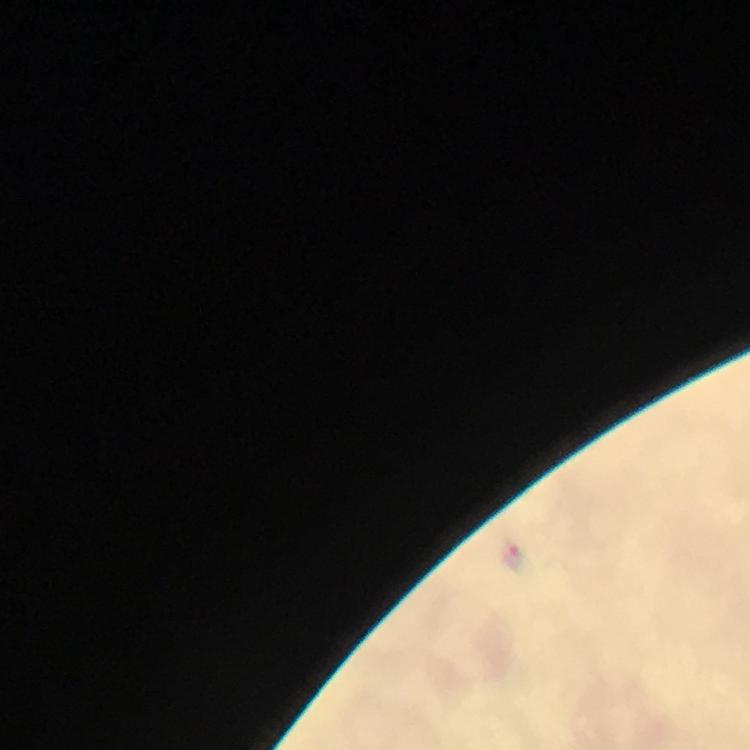

cropped from = one field of view
immersion oil = used
context = from a malaria diagnostic workup
preparation = thick blood film
malaria parasite locations = approximate object centers, in pixels from the top-left corner: (x=514, y=558)
image size = 750×750 pixels
stain = Giemsa
capture = smartphone photograph through a microscope
magnification = 100x